Name the blood parasite species.
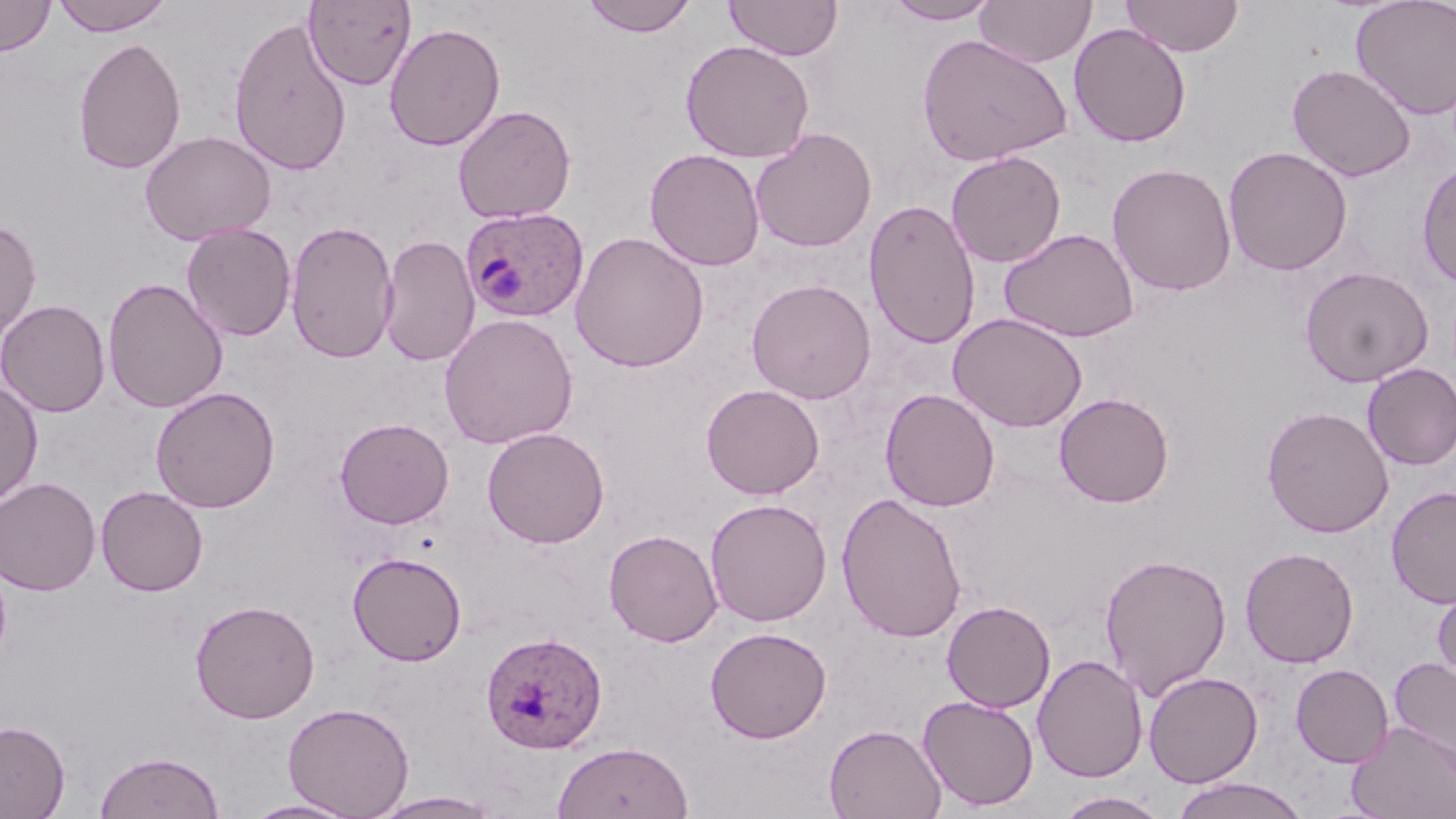

Plasmodium ovale.

Summary:
  - Coordinate format: approximate bounding boxes as [x1, y1, x2, y2] in pixels
  - Uninfected red blood cell locations: [0, 0, 56, 56], [50, 0, 174, 36], [304, 0, 416, 90], [579, 0, 698, 37], [725, 0, 843, 60], [882, 0, 1002, 25], [974, 0, 1096, 68], [1121, 0, 1244, 57], [1350, 0, 1456, 120], [228, 13, 352, 176], [384, 22, 506, 151], [1068, 23, 1192, 147], [916, 33, 1073, 167], [73, 36, 186, 175], [680, 40, 815, 163], [1287, 63, 1417, 181], [453, 104, 576, 224], [750, 127, 877, 252], [140, 129, 276, 246], [1223, 146, 1353, 275], [644, 148, 765, 270], [946, 150, 1066, 268], [1417, 161, 1456, 287], [1107, 163, 1237, 296], [863, 199, 981, 350], [0, 218, 41, 343], [285, 219, 399, 363], [181, 223, 297, 341], [999, 228, 1139, 342], [570, 230, 709, 373], [378, 234, 479, 366], [1299, 265, 1434, 388], [102, 277, 228, 414], [746, 278, 876, 404], [0, 298, 111, 418], [949, 312, 1088, 432], [439, 313, 579, 449], [1361, 363, 1456, 470], [0, 380, 43, 508], [701, 383, 825, 499], [150, 386, 281, 513], [880, 388, 1000, 512], [1054, 392, 1175, 508], [1261, 405, 1395, 538], [335, 417, 454, 529], [482, 426, 610, 548], [0, 477, 101, 596], [95, 485, 208, 596], [1386, 486, 1456, 608], [836, 491, 967, 643], [705, 498, 832, 626], [604, 529, 723, 646], [1239, 546, 1359, 668], [347, 551, 467, 665], [1099, 553, 1233, 698], [0, 555, 12, 669], [1432, 580, 1456, 689], [189, 599, 320, 724], [941, 600, 1056, 712], [704, 626, 832, 743], [1032, 654, 1148, 782], [1389, 657, 1456, 774], [1290, 663, 1394, 767], [1144, 671, 1263, 787], [917, 695, 1039, 811], [282, 702, 415, 818], [0, 720, 71, 819], [1347, 721, 1456, 818], [824, 723, 946, 819], [552, 741, 693, 819], [94, 751, 225, 818], [1170, 777, 1310, 819], [368, 791, 503, 818], [1054, 791, 1170, 819], [241, 798, 364, 818]
  - Plasmodium ovale-infected red blood cell locations: [461, 207, 589, 322], [480, 630, 608, 753]
  - Magnification: 1000x
  - Preparation: thin blood smear
  - Stain: May-Grünwald-Giemsa
  - Field of view: single
  - Modality: optical microscopy
  - Image size: 1456×819 pixels